Give the position of every leukocyte visible.
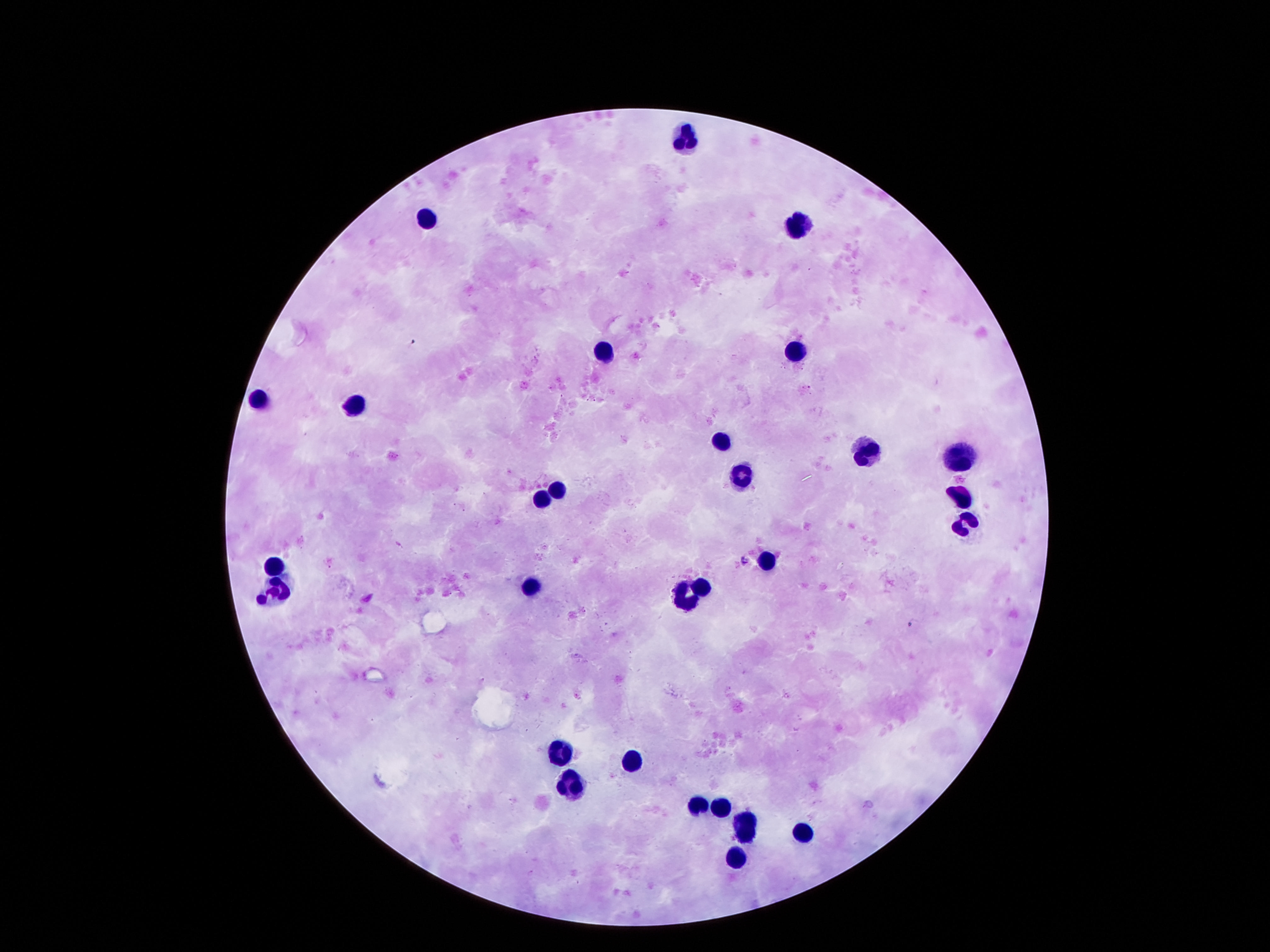

Approximate centers as [x, y] in pixels.
Leukocytes: [684, 133], [424, 220], [800, 220], [603, 350], [794, 353], [259, 400], [354, 403], [721, 442], [965, 452], [868, 453], [742, 470], [558, 485], [960, 494], [540, 498], [965, 524], [763, 558], [275, 561], [529, 584], [703, 584], [275, 596], [682, 596], [556, 752], [632, 757], [569, 775], [697, 806], [721, 809], [745, 822], [805, 830], [737, 859].

Patient malaria status: negative. Giemsa-stained preparation. Single field of view. Thick blood smear. 100x magnification. Photographed through the microscope eyepiece with a smartphone camera. Image is 1270×952 pixels.